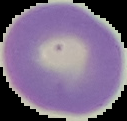
malaria status = uninfected
image type = segmented cell region with the area outside set to black
image size = 127×121 pixels
preparation = thin blood smear